Outline each blood parasite and name the species.
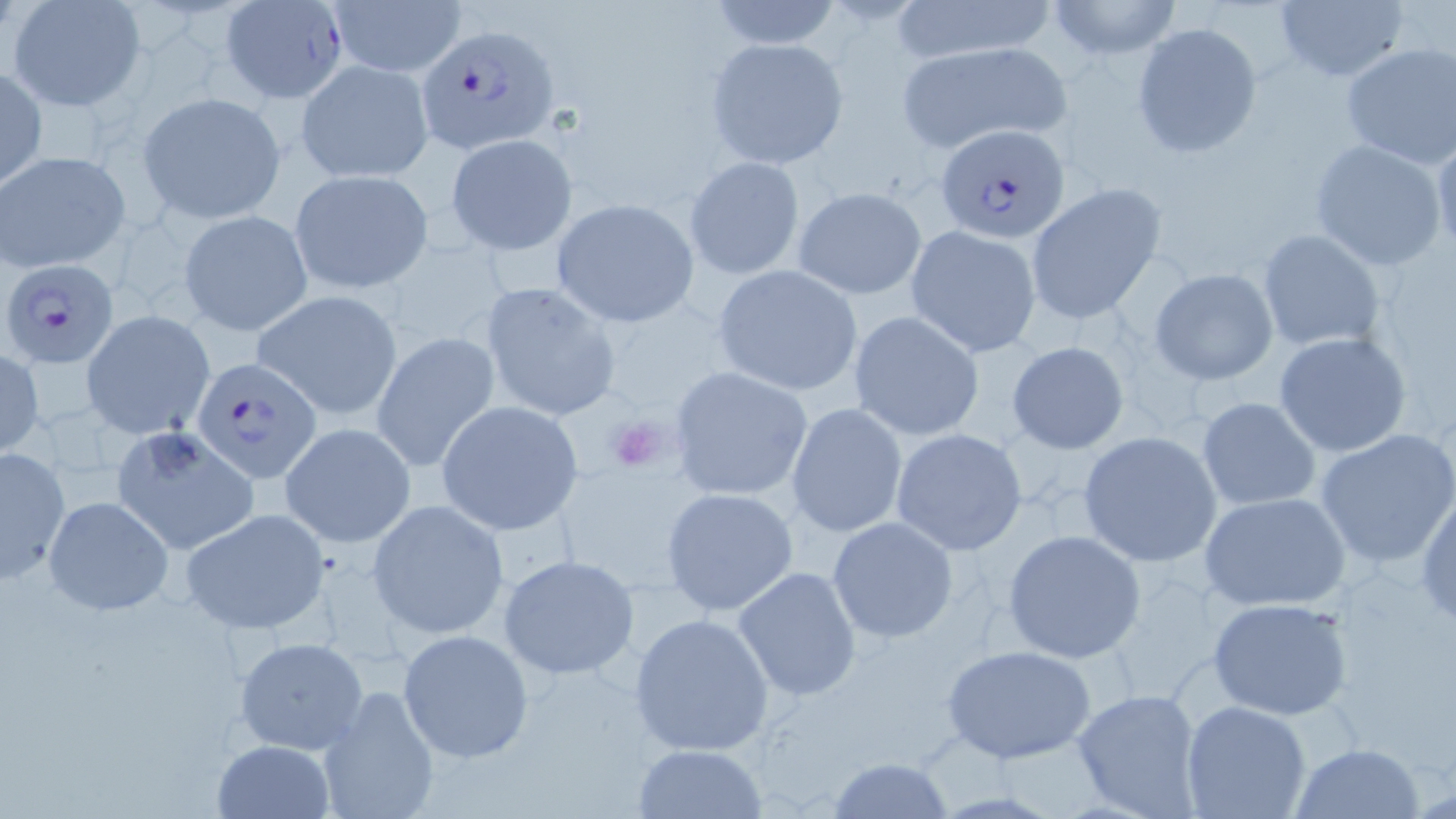
Approximate bounding boxes as (x1,y1)-(x2,y2) corner pairs in pixels.
Plasmodium falciparum-infected red blood cells: (221,0)-(353,100), (418,23)-(561,152), (937,124)-(1070,244), (4,258)-(120,366), (191,355)-(322,483).
No Plasmodium ovale, Plasmodium malariae, Plasmodium vivax, Babesia divergens, or Trypanosoma brucei observed.

Summary:
  - Uninfected red blood cell locations: (703,0)-(847,51), (886,0)-(1061,64), (1045,0)-(1183,60), (8,1)-(147,112), (327,1)-(467,77), (1272,1)-(1409,83), (1131,22)-(1261,158), (704,38)-(848,169), (895,39)-(1074,152), (1340,42)-(1456,168), (297,58)-(434,184), (0,66)-(46,189), (138,91)-(285,222), (445,131)-(578,256), (1431,135)-(1456,262), (1309,139)-(1448,272), (0,151)-(130,273), (684,156)-(805,280), (289,168)-(432,293), (1025,182)-(1167,325), (793,186)-(926,299), (550,197)-(701,325), (753,202)-(905,351), (178,209)-(314,337), (905,226)-(1042,357), (1257,229)-(1385,353), (710,265)-(865,397), (1149,268)-(1279,385), (479,280)-(623,423), (252,289)-(404,419), (82,310)-(215,441), (847,311)-(987,441), (372,331)-(501,475), (1272,332)-(1411,458), (1006,341)-(1130,454), (0,351)-(44,455), (667,366)-(813,501), (1196,397)-(1322,511), (437,400)-(585,535), (787,403)-(907,538), (280,421)-(415,548), (111,423)-(259,556), (891,428)-(1028,556), (1315,429)-(1456,568), (1077,431)-(1223,568), (0,447)-(71,583), (661,487)-(798,616), (1416,488)-(1456,630), (1199,490)-(1352,611), (42,495)-(173,615), (367,499)-(510,641), (180,508)-(330,635), (695,511)-(834,667), (827,517)-(960,643), (1002,528)-(1146,664), (499,555)-(638,680), (732,566)-(860,703), (1207,597)-(1354,720), (628,612)-(776,758), (397,630)-(534,763), (233,637)-(368,754), (942,643)-(1097,765), (316,685)-(440,819), (1071,686)-(1205,818), (1181,701)-(1311,819), (209,739)-(335,819), (1291,741)-(1425,818), (632,743)-(766,817), (828,756)-(954,819)
  - Platelet locations: (600,407)-(678,475)
  - Slide-level diagnosis: Plasmodium falciparum
  - Field of view: single
  - Modality: light microscopy
  - Image size: 1456×819 pixels
  - Magnification: 1000x
  - Stain: May-Grünwald-Giemsa
  - Preparation: thin blood film